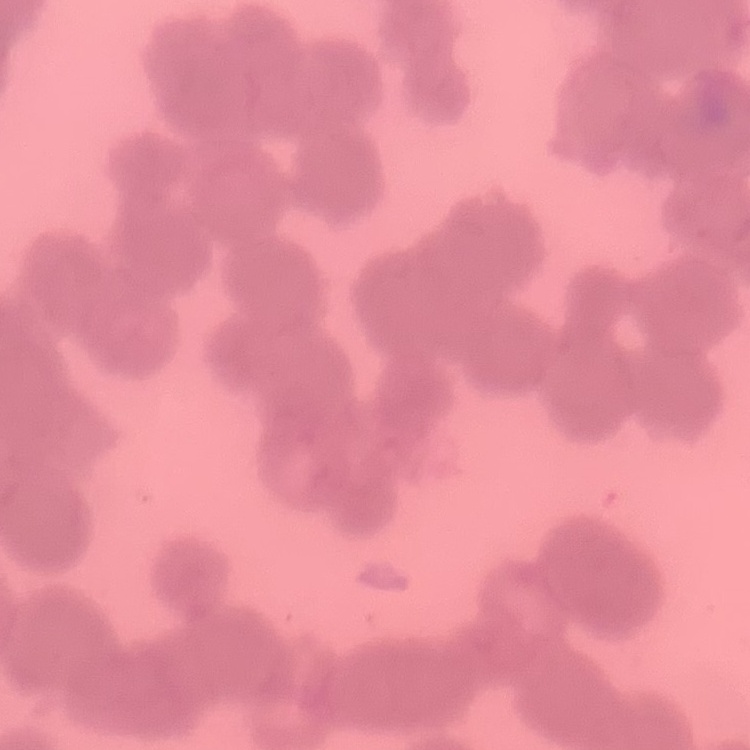

Summary:
  - Red blood cell morphology: rouleaux formation
  - Preparation: thin peripheral smear
  - Stain: Field's or Giemsa
  - Image type: square crop of a larger photomicrograph